Assess this cell for malaria.
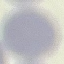

Uninfected.

Acquired by smartphone through the microscope eyepiece. Giemsa stain. Thin blood film. Cell patch, automatically extracted from a larger field of view and resized to 64 × 64 pixels.